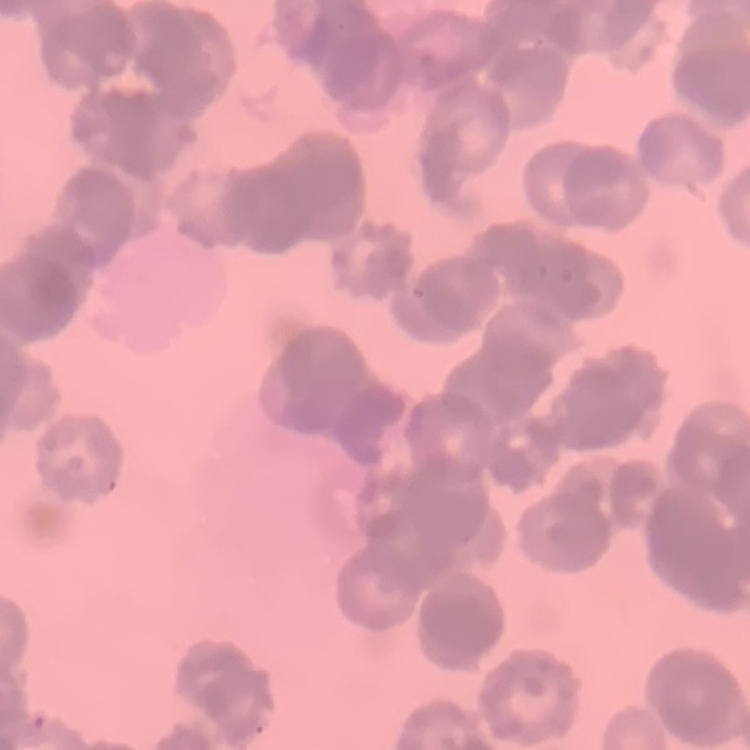

red blood cell morphology = rouleaux formation
stain = Field's or Giemsa
image type = square crop of a larger photomicrograph
preparation = thin blood film